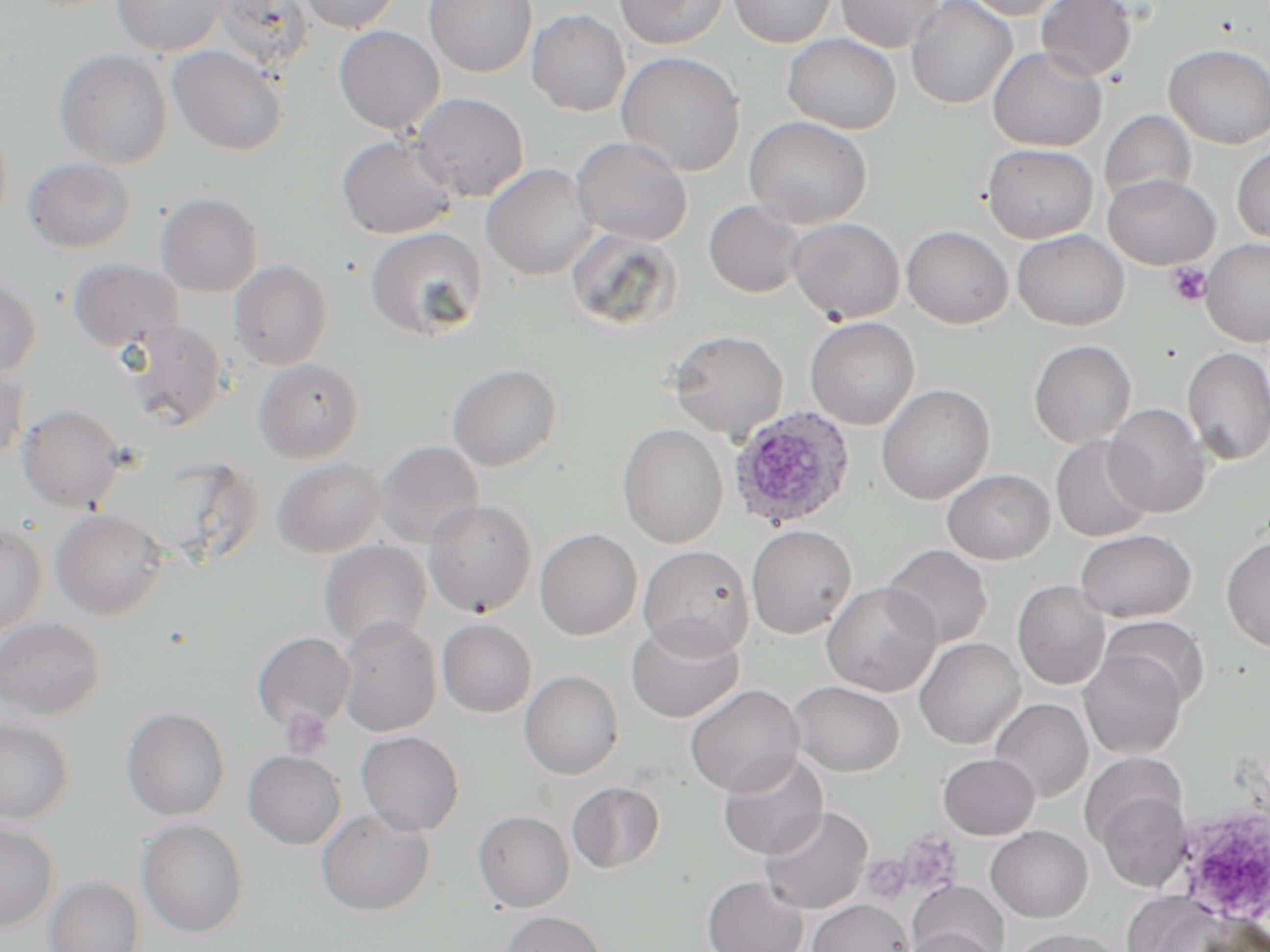

slide-level diagnosis = Plasmodium ovale
field of view = one of a larger specimen
Plasmodium ovale-infected red blood cell locations = approximate bounding boxes as (x1,y1)-(x2,y2) corner pairs in pixels: (727,405)-(857,531)
uninfected red blood cell locations = approximate bounding boxes as (x1,y1)-(x2,y2) corner pairs in pixels: (111,0)-(228,57), (296,0)-(403,34), (424,0)-(538,78), (614,0)-(728,50), (727,0)-(836,48), (835,0)-(946,53), (906,0)-(1018,109), (962,0)-(1074,20), (1036,0)-(1137,81), (211,1)-(315,72), (527,9)-(630,116), (334,26)-(444,134), (782,34)-(901,134), (1164,43)-(1270,148), (167,45)-(288,156), (987,47)-(1107,151), (53,48)-(173,169), (615,51)-(746,176), (412,93)-(530,201), (1098,110)-(1197,204), (744,116)-(872,227), (336,134)-(458,240), (571,136)-(692,245), (982,143)-(1099,243), (1232,144)-(1270,244), (22,157)-(136,253), (481,164)-(596,281), (1102,173)-(1220,269), (154,191)-(263,298), (704,200)-(808,298), (786,217)-(905,323), (901,225)-(1014,328), (365,226)-(488,339), (569,229)-(686,331), (1012,229)-(1129,331), (1200,239)-(1270,347), (67,258)-(184,353), (229,259)-(333,369), (0,274)-(42,380), (804,316)-(919,429), (121,319)-(231,430), (666,329)-(788,440), (1028,340)-(1136,448), (1182,347)-(1270,465), (253,357)-(364,464), (0,361)-(29,463), (446,363)-(562,471), (876,384)-(995,505), (17,402)-(127,513), (1103,403)-(1210,518), (616,423)-(729,548), (1051,436)-(1153,542), (373,440)-(484,548), (271,456)-(388,558), (942,468)-(1055,564), (422,499)-(537,618), (50,509)-(167,619), (0,522)-(48,637), (745,524)-(857,639), (1075,528)-(1197,622), (534,529)-(642,640), (1221,537)-(1270,651), (319,540)-(433,649), (882,544)-(993,649), (637,545)-(754,659), (1012,580)-(1110,690), (821,582)-(941,697), (1099,615)-(1209,707), (335,616)-(442,737), (0,617)-(106,721), (349,618)-(454,835), (437,618)-(537,717), (625,618)-(744,723), (252,631)-(356,733), (914,637)-(1026,749), (1078,650)-(1187,759), (519,670)-(624,779), (789,680)-(904,777), (685,683)-(804,797), (990,697)-(1093,802), (121,706)-(231,821), (0,718)-(74,824), (356,730)-(465,836), (241,742)-(460,847), (243,750)-(346,849), (718,752)-(828,860), (938,753)-(1040,840), (567,781)-(665,873), (1091,783)-(1191,893), (759,805)-(872,914), (316,807)-(435,915), (472,810)-(575,912), (137,819)-(249,937), (0,822)-(58,930), (985,825)-(1092,922), (702,876)-(807,952), (44,877)-(144,952), (909,882)-(1009,951), (1123,893)-(1228,951), (807,899)-(912,952), (498,910)-(608,952), (901,927)-(1000,952), (1008,927)-(1127,952)
platelet locations = approximate bounding boxes as (x1,y1)-(x2,y2) corner pairs in pixels: (1166,263)-(1212,307), (281,708)-(333,760), (1171,802)-(1269,924), (897,830)-(963,897), (863,855)-(911,904)
image size = 1270×952 pixels
preparation = thin blood film
modality = optical microscopy
magnification = 1000x
stain = May-Grünwald-Giemsa